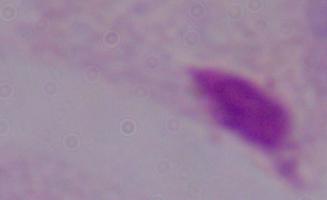

{
  "identification": "trichomonad",
  "magnification": "1000x",
  "modality": "micrograph"
}